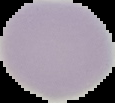
Summary:
  - Preparation: thin blood film
  - Image size: 115×103 pixels
  - Image type: cell region segmented out of the field of view; surrounding area masked to black
  - Malaria status: uninfected